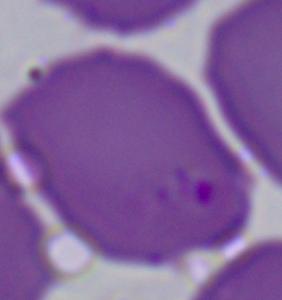

Summary:
  - Identification: Babesia
  - Modality: micrograph
  - Magnification: 1000x